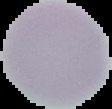
Summary:
  - Image size: 112×109 pixels
  - Result: no Plasmodium parasites detected
  - Preparation: thin blood film
  - Image type: segmented cell region on a black background